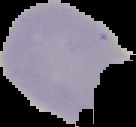
Segmented cell region on a black background. Image is 136×127 pixels. Result: Plasmodium parasites identified. From a thin blood smear.